Classify this cell by malaria status.
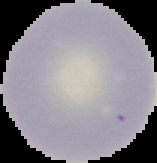
Uninfected.

image_type: segmented cell region on a black background
preparation: thin blood film
image_size: 157×163 pixels